Assess the morphology of the erythrocytes.
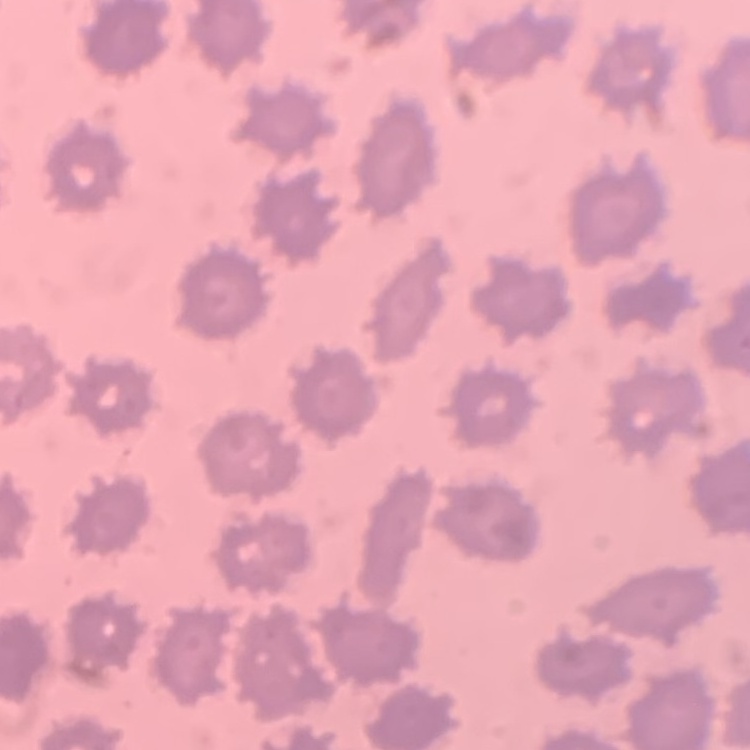

No rouleaux formation.

image type = square crop of a larger photomicrograph
preparation = thin blood smear
stain = Field's or Giemsa